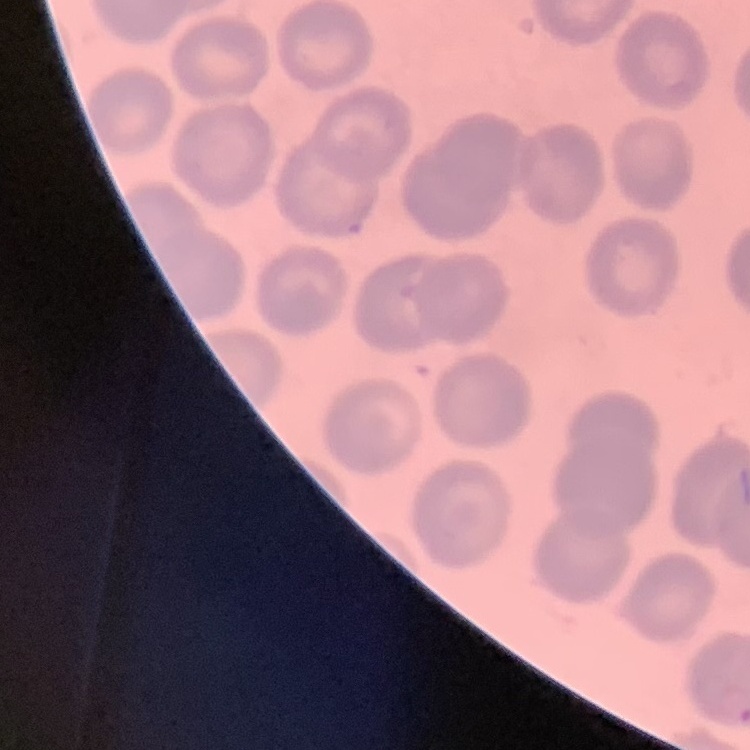
The red blood cells exhibit no rouleaux formation. Field's or Giemsa stain. Square crop of a larger photomicrograph. Thin blood smear.